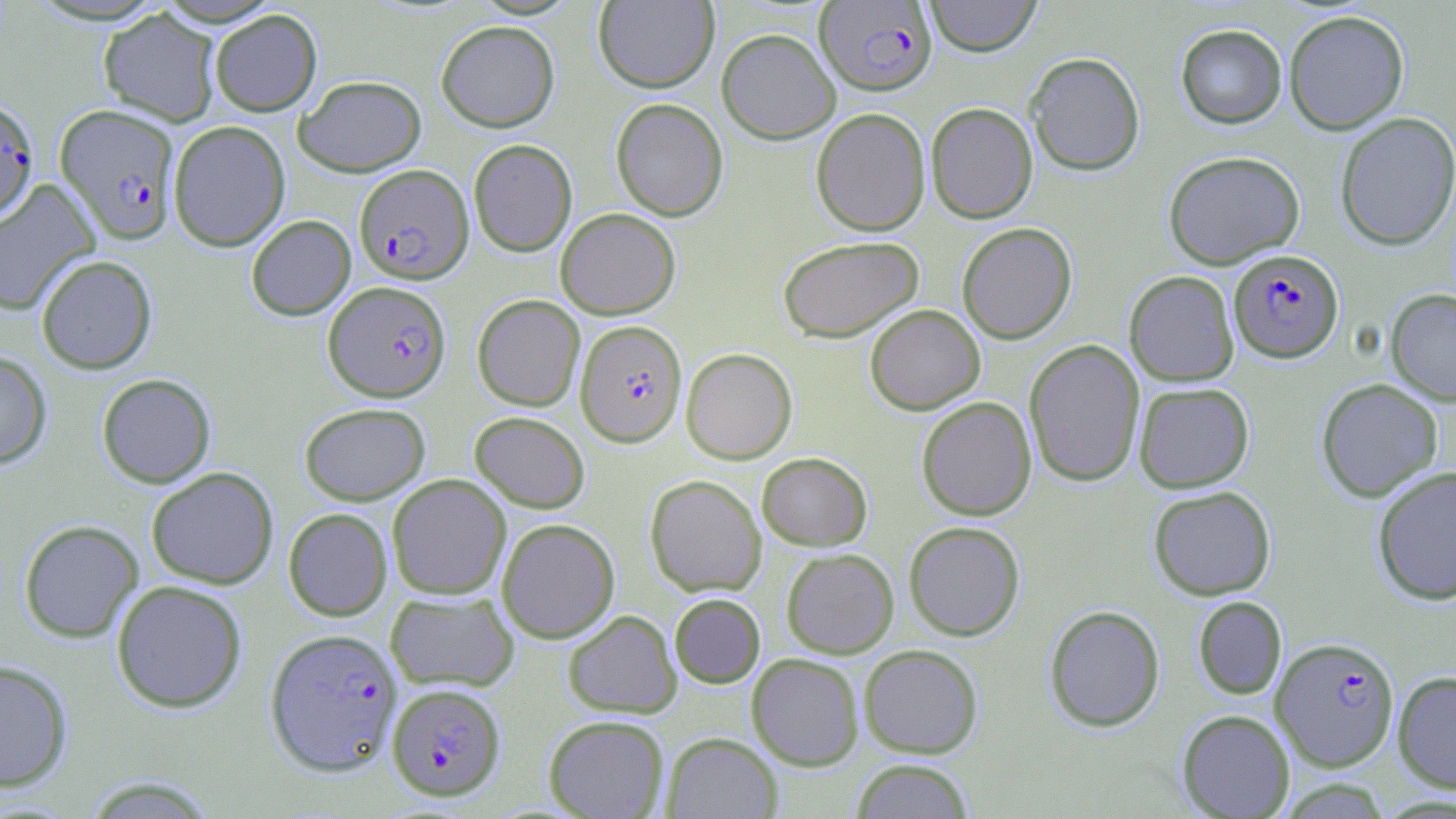

Approximate bounding boxes as (x1,y1)-(x2,y2) corner pairs in pixels. Uninfected red blood cell locations: (924,0)-(1042,57), (593,1)-(719,93), (98,8)-(221,126), (210,9)-(322,116), (1284,10)-(1409,134), (436,20)-(560,132), (1175,24)-(1287,129), (716,28)-(841,144), (1025,52)-(1145,176), (295,75)-(426,176), (610,97)-(728,221), (925,102)-(1038,223), (811,108)-(931,236), (1334,112)-(1456,251), (168,120)-(290,251), (468,138)-(577,256), (1163,150)-(1305,269), (0,179)-(101,316), (555,208)-(680,319), (246,215)-(356,320), (957,222)-(1077,344), (778,235)-(924,343), (36,254)-(157,374), (1124,271)-(1239,386), (1386,288)-(1456,406), (472,294)-(585,411), (865,304)-(985,415), (1024,339)-(1145,487), (681,347)-(797,464), (0,351)-(52,469), (96,373)-(216,488), (1315,378)-(1444,503), (1133,381)-(1255,493), (916,397)-(1037,521), (299,402)-(430,505), (470,411)-(590,513), (757,452)-(872,550), (1372,466)-(1456,605), (146,467)-(279,589), (387,474)-(511,599), (645,474)-(767,597), (1148,485)-(1276,600), (283,508)-(393,621), (496,517)-(620,643), (18,519)-(144,642), (904,521)-(1025,640), (781,547)-(899,658), (111,580)-(248,713), (385,590)-(519,692), (669,593)-(765,688), (1193,596)-(1287,700), (1044,604)-(1165,732), (562,610)-(682,718), (859,644)-(984,758), (746,653)-(864,770), (0,659)-(73,791), (1393,670)-(1456,793), (1176,709)-(1295,818), (543,714)-(669,818), (662,732)-(782,819), (851,759)-(975,819), (81,775)-(219,818). Plasmodium falciparum-infected red blood cell locations: (816,1)-(937,95), (0,98)-(39,221), (56,104)-(180,244), (355,164)-(474,284), (1229,249)-(1343,362), (323,280)-(452,401), (575,319)-(687,447), (265,628)-(403,776), (1271,636)-(1400,772), (387,683)-(506,801). Slide-level diagnosis: Plasmodium falciparum. Thin blood smear. Optical microscopy. Image is 1456×819 pixels. May-Grünwald-Giemsa-stained preparation. Single field of view. 1000x magnification.